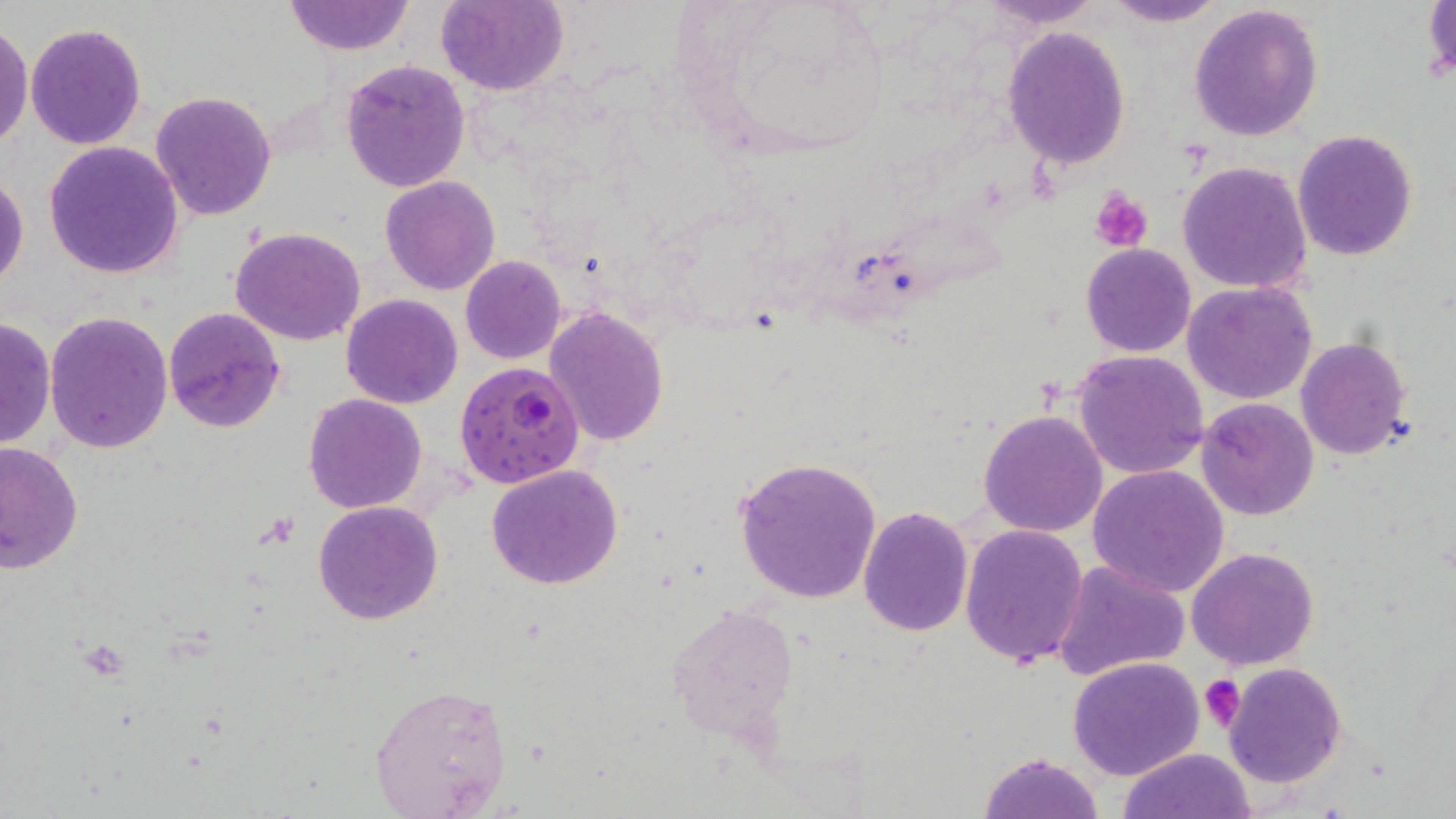
{
  "slide_level_diagnosis": "Plasmodium falciparum",
  "preparation": "thin blood smear",
  "magnification": "1000x",
  "uninfected_red_blood_cell_locations": "approximate bounding boxes as named x1/y1/x2/y2 corners in pixels: (x1=436, y1=0, x2=569, y2=96), (x1=977, y1=0, x2=1107, y2=28), (x1=1102, y1=0, x2=1226, y2=27), (x1=282, y1=1, x2=415, y2=55), (x1=1423, y1=2, x2=1455, y2=86), (x1=1190, y1=3, x2=1324, y2=141), (x1=25, y1=22, x2=148, y2=150), (x1=0, y1=24, x2=32, y2=149), (x1=1001, y1=27, x2=1131, y2=168), (x1=341, y1=59, x2=471, y2=195), (x1=150, y1=91, x2=277, y2=222), (x1=1292, y1=130, x2=1419, y2=261), (x1=43, y1=142, x2=184, y2=281), (x1=1176, y1=159, x2=1315, y2=295), (x1=0, y1=173, x2=27, y2=292), (x1=381, y1=175, x2=501, y2=295), (x1=230, y1=227, x2=368, y2=347), (x1=1081, y1=244, x2=1196, y2=357), (x1=461, y1=254, x2=566, y2=365), (x1=1183, y1=281, x2=1317, y2=404), (x1=341, y1=294, x2=464, y2=409), (x1=164, y1=307, x2=286, y2=431), (x1=544, y1=307, x2=670, y2=447), (x1=44, y1=310, x2=173, y2=453), (x1=0, y1=314, x2=55, y2=452), (x1=1295, y1=335, x2=1414, y2=459), (x1=1073, y1=349, x2=1209, y2=478), (x1=304, y1=394, x2=426, y2=513), (x1=1196, y1=396, x2=1320, y2=521), (x1=978, y1=409, x2=1109, y2=537), (x1=0, y1=443, x2=83, y2=572), (x1=733, y1=454, x2=882, y2=604), (x1=486, y1=464, x2=623, y2=589), (x1=1088, y1=464, x2=1230, y2=597), (x1=313, y1=500, x2=442, y2=624), (x1=859, y1=506, x2=973, y2=635), (x1=959, y1=524, x2=1089, y2=668), (x1=1187, y1=545, x2=1319, y2=669), (x1=1052, y1=560, x2=1192, y2=682), (x1=666, y1=600, x2=800, y2=747), (x1=1067, y1=655, x2=1206, y2=779), (x1=1224, y1=662, x2=1346, y2=787), (x1=369, y1=680, x2=514, y2=817), (x1=1118, y1=748, x2=1256, y2=819), (x1=979, y1=749, x2=1105, y2=819)",
  "stain": "May-Grünwald-Giemsa",
  "field_of_view": "single",
  "modality": "optical microscopy",
  "plasmodium_falciparum_infected_red_blood_cell_locations": "approximate bounding boxes as named x1/y1/x2/y2 corners in pixels: (x1=455, y1=361, x2=583, y2=486)",
  "platelet_locations": "approximate bounding boxes as named x1/y1/x2/y2 corners in pixels: (x1=1090, y1=187, x2=1151, y2=252), (x1=1200, y1=673, x2=1245, y2=733)",
  "image_size": "1456×819 pixels"
}